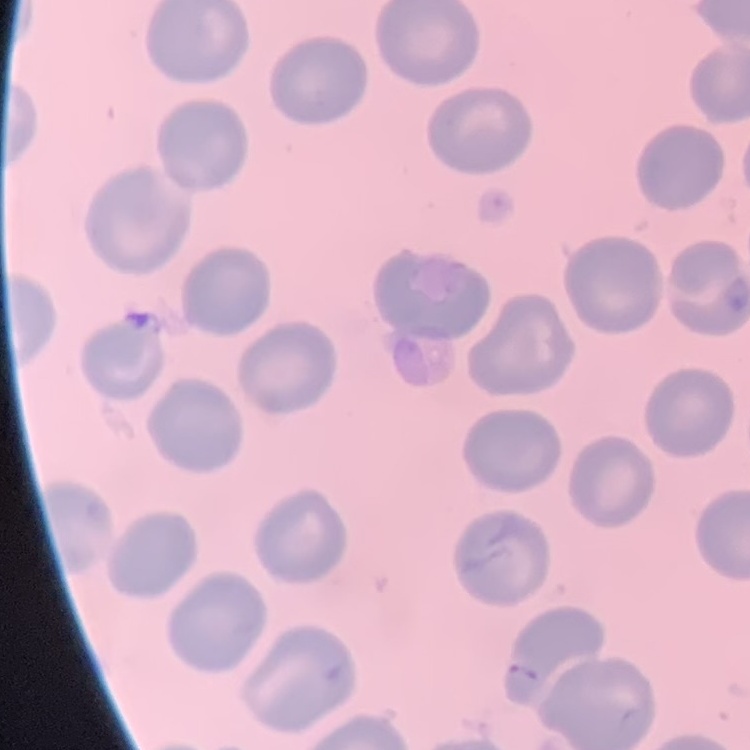

The erythrocytes exhibit no rouleaux formation. Thin peripheral smear. Square crop of a larger photomicrograph. Field's or Giemsa stain.